Outline each blood parasite and name the species.
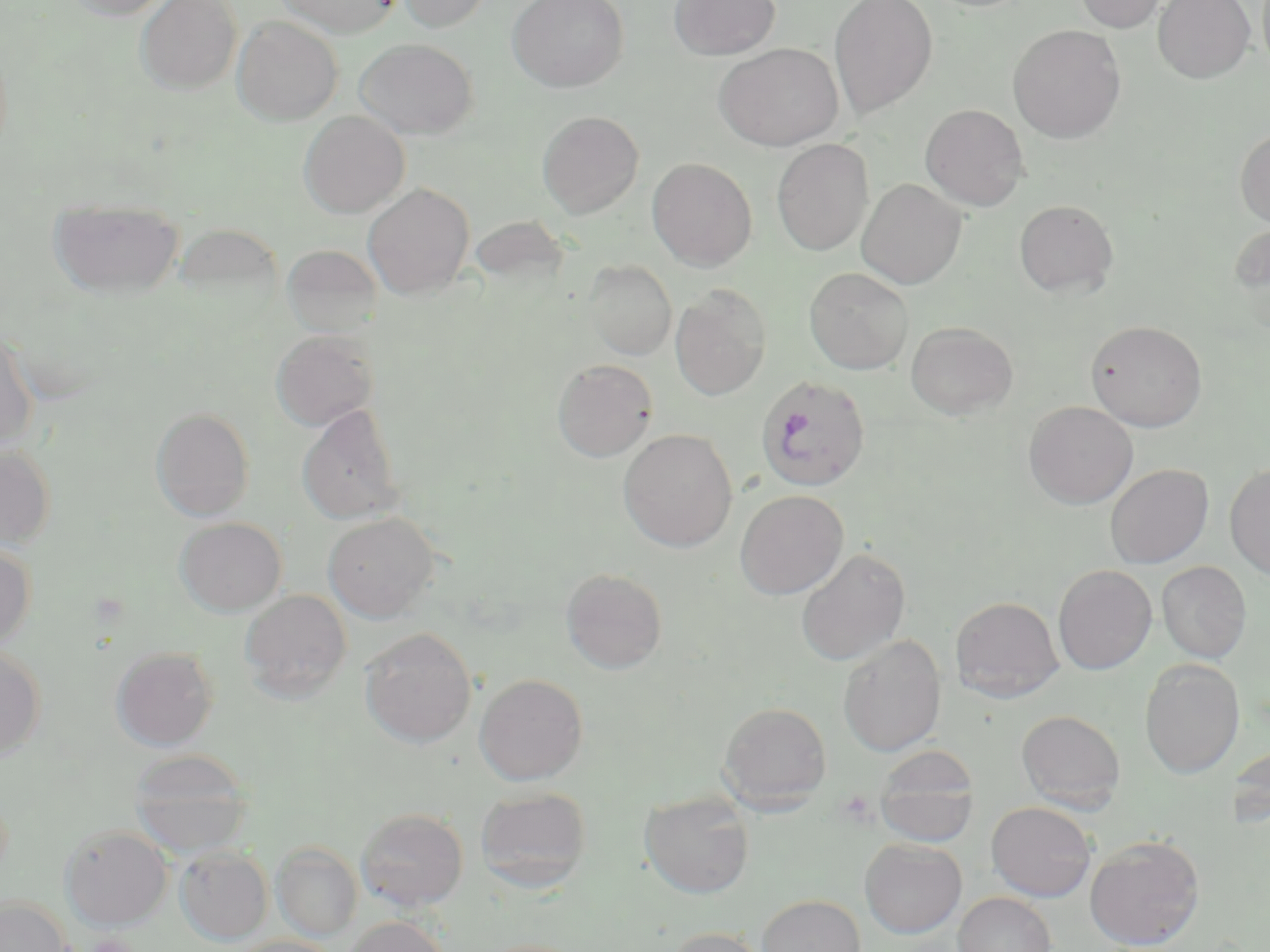

Approximate bounding boxes as (x1, y1, x2, y2) in pixels.
Plasmodium falciparum-infected red blood cells: (755, 375, 871, 492).
No Plasmodium ovale, Plasmodium malariae, Plasmodium vivax, Babesia divergens, or Trypanosoma brucei observed.

Summary:
  - Platelet locations: (86, 934, 137, 952)
  - Uninfected red blood cell locations: (64, 0, 175, 20), (135, 0, 242, 95), (274, 0, 402, 38), (396, 0, 495, 32), (507, 0, 629, 92), (669, 0, 780, 60), (829, 0, 938, 119), (1072, 0, 1169, 33), (1153, 0, 1255, 83), (1259, 0, 1270, 75), (232, 15, 343, 125), (1007, 24, 1126, 143), (354, 38, 478, 139), (714, 43, 843, 150), (920, 103, 1030, 211), (537, 110, 644, 217), (299, 111, 409, 218), (1235, 126, 1270, 229), (771, 139, 874, 256), (646, 157, 757, 271), (857, 178, 966, 289), (363, 182, 475, 299), (49, 198, 184, 299), (1014, 199, 1118, 297), (1228, 221, 1270, 332), (283, 245, 381, 337), (583, 260, 677, 361), (804, 267, 914, 374), (670, 284, 772, 401), (1086, 319, 1207, 432), (905, 321, 1018, 420), (0, 324, 38, 451), (271, 330, 377, 431), (553, 359, 658, 461), (1023, 400, 1138, 509), (297, 404, 405, 525), (151, 407, 255, 521), (618, 428, 738, 552), (0, 443, 56, 549), (1105, 463, 1213, 568), (1224, 463, 1270, 580), (735, 489, 849, 599), (322, 512, 440, 622), (174, 517, 287, 616), (0, 542, 37, 651), (796, 548, 911, 666), (1156, 561, 1251, 663), (1053, 564, 1157, 674), (561, 568, 667, 674), (240, 589, 352, 701), (950, 596, 1064, 703), (359, 627, 477, 747), (838, 634, 946, 757), (0, 644, 47, 761), (111, 646, 219, 750), (1139, 658, 1245, 778), (474, 673, 588, 785), (718, 701, 832, 810), (1016, 709, 1126, 812), (1229, 742, 1269, 828), (874, 746, 980, 847), (129, 750, 254, 856), (475, 786, 591, 892), (639, 791, 755, 898), (986, 801, 1097, 902), (356, 808, 468, 911), (60, 824, 172, 930), (1084, 834, 1205, 950), (860, 838, 966, 938), (272, 842, 362, 941), (175, 847, 272, 944), (954, 891, 1057, 952), (757, 894, 866, 952), (0, 896, 72, 952), (342, 916, 449, 952), (665, 926, 769, 952), (231, 935, 341, 952), (476, 939, 588, 952)
  - Slide-level diagnosis: Plasmodium falciparum
  - Magnification: 1000x
  - Field of view: one of a larger specimen
  - Image size: 1270×952 pixels
  - Modality: optical microscopy
  - Preparation: thin blood film
  - Stain: May-Grünwald-Giemsa